State the blood parasite species.
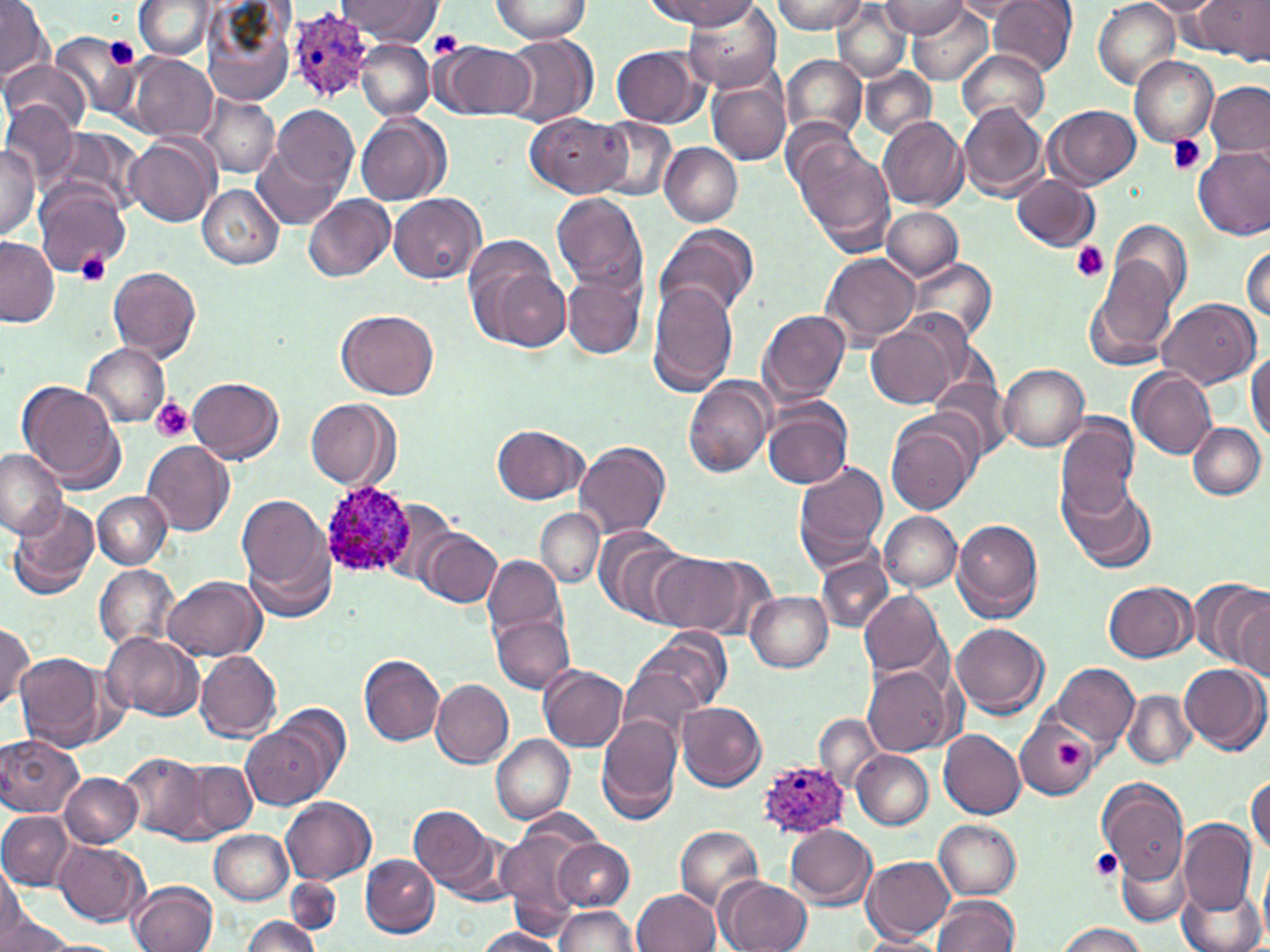
Plasmodium ovale.

Approximate bounding boxes as named x1/y1/x2/y2 corners in pixels. Plasmodium ovale-infected red blood cell locations: (x1=289, y1=6, x2=379, y2=100), (x1=317, y1=482, x2=418, y2=579), (x1=754, y1=757, x2=850, y2=841). Uninfected red blood cell locations: (x1=338, y1=0, x2=441, y2=43), (x1=490, y1=0, x2=591, y2=42), (x1=647, y1=0, x2=764, y2=29), (x1=772, y1=0, x2=868, y2=34), (x1=953, y1=0, x2=1038, y2=20), (x1=989, y1=0, x2=1077, y2=76), (x1=1138, y1=0, x2=1227, y2=17), (x1=1195, y1=0, x2=1267, y2=61), (x1=0, y1=1, x2=52, y2=81), (x1=133, y1=1, x2=215, y2=61), (x1=1093, y1=2, x2=1180, y2=86), (x1=199, y1=3, x2=295, y2=108), (x1=685, y1=3, x2=782, y2=91), (x1=831, y1=3, x2=910, y2=82), (x1=878, y1=3, x2=969, y2=36), (x1=904, y1=4, x2=995, y2=83), (x1=50, y1=30, x2=143, y2=121), (x1=502, y1=34, x2=597, y2=128), (x1=356, y1=39, x2=435, y2=121), (x1=434, y1=40, x2=533, y2=121), (x1=611, y1=46, x2=707, y2=126), (x1=957, y1=49, x2=1049, y2=130), (x1=127, y1=53, x2=219, y2=141), (x1=782, y1=54, x2=869, y2=143), (x1=1128, y1=55, x2=1217, y2=146), (x1=1, y1=58, x2=86, y2=135), (x1=861, y1=66, x2=937, y2=140), (x1=708, y1=77, x2=791, y2=165), (x1=1206, y1=81, x2=1270, y2=157), (x1=195, y1=94, x2=278, y2=178), (x1=0, y1=103, x2=80, y2=190), (x1=957, y1=103, x2=1049, y2=201), (x1=1045, y1=104, x2=1140, y2=188), (x1=270, y1=105, x2=357, y2=194), (x1=526, y1=111, x2=632, y2=197), (x1=356, y1=113, x2=450, y2=206), (x1=878, y1=115, x2=969, y2=210), (x1=780, y1=116, x2=870, y2=209), (x1=593, y1=119, x2=677, y2=202), (x1=46, y1=126, x2=144, y2=220), (x1=124, y1=132, x2=219, y2=228), (x1=794, y1=138, x2=894, y2=254), (x1=659, y1=142, x2=743, y2=227), (x1=0, y1=143, x2=41, y2=240), (x1=1194, y1=144, x2=1270, y2=240), (x1=252, y1=148, x2=342, y2=229), (x1=1012, y1=174, x2=1102, y2=253), (x1=34, y1=181, x2=134, y2=277), (x1=197, y1=184, x2=284, y2=271), (x1=552, y1=191, x2=648, y2=294), (x1=388, y1=192, x2=487, y2=285), (x1=305, y1=195, x2=394, y2=281), (x1=882, y1=208, x2=964, y2=281), (x1=1110, y1=218, x2=1193, y2=313), (x1=655, y1=223, x2=758, y2=321), (x1=0, y1=237, x2=57, y2=325), (x1=463, y1=237, x2=569, y2=351), (x1=1242, y1=240, x2=1270, y2=326), (x1=820, y1=252, x2=921, y2=347), (x1=907, y1=257, x2=998, y2=345), (x1=1089, y1=259, x2=1179, y2=366), (x1=108, y1=266, x2=201, y2=361), (x1=561, y1=269, x2=648, y2=360), (x1=646, y1=280, x2=740, y2=393), (x1=1156, y1=299, x2=1260, y2=390), (x1=758, y1=308, x2=852, y2=408), (x1=337, y1=309, x2=439, y2=401), (x1=865, y1=315, x2=967, y2=410), (x1=83, y1=344, x2=172, y2=428), (x1=1246, y1=349, x2=1270, y2=442), (x1=998, y1=365, x2=1089, y2=452), (x1=1128, y1=367, x2=1217, y2=460), (x1=186, y1=375, x2=284, y2=464), (x1=928, y1=375, x2=1015, y2=464), (x1=683, y1=377, x2=775, y2=478), (x1=17, y1=380, x2=125, y2=492), (x1=304, y1=396, x2=400, y2=490), (x1=761, y1=401, x2=851, y2=490), (x1=1055, y1=413, x2=1141, y2=516), (x1=886, y1=414, x2=978, y2=515), (x1=1189, y1=421, x2=1266, y2=499), (x1=492, y1=424, x2=588, y2=504), (x1=142, y1=440, x2=235, y2=535), (x1=574, y1=441, x2=671, y2=539), (x1=0, y1=450, x2=66, y2=537), (x1=794, y1=461, x2=889, y2=568), (x1=1059, y1=475, x2=1158, y2=575), (x1=94, y1=491, x2=171, y2=568), (x1=238, y1=494, x2=332, y2=601), (x1=381, y1=498, x2=461, y2=589), (x1=6, y1=500, x2=98, y2=598), (x1=535, y1=508, x2=603, y2=588), (x1=878, y1=512, x2=963, y2=591), (x1=952, y1=520, x2=1043, y2=623), (x1=591, y1=528, x2=698, y2=625), (x1=421, y1=529, x2=502, y2=608), (x1=650, y1=554, x2=754, y2=635), (x1=483, y1=555, x2=566, y2=640), (x1=816, y1=555, x2=892, y2=633), (x1=94, y1=564, x2=179, y2=653), (x1=162, y1=575, x2=267, y2=662), (x1=1189, y1=579, x2=1270, y2=671), (x1=1104, y1=582, x2=1198, y2=662), (x1=858, y1=589, x2=947, y2=680), (x1=746, y1=592, x2=832, y2=673), (x1=1228, y1=592, x2=1269, y2=679), (x1=490, y1=613, x2=573, y2=694), (x1=0, y1=622, x2=36, y2=709), (x1=950, y1=622, x2=1048, y2=718), (x1=637, y1=628, x2=731, y2=715), (x1=102, y1=631, x2=204, y2=721), (x1=16, y1=652, x2=107, y2=749), (x1=196, y1=652, x2=281, y2=743), (x1=359, y1=655, x2=445, y2=745), (x1=1179, y1=661, x2=1269, y2=755), (x1=1051, y1=663, x2=1139, y2=750), (x1=538, y1=664, x2=628, y2=751), (x1=865, y1=665, x2=955, y2=756), (x1=619, y1=667, x2=703, y2=748), (x1=430, y1=679, x2=514, y2=768), (x1=1122, y1=690, x2=1196, y2=769), (x1=271, y1=700, x2=349, y2=794), (x1=677, y1=702, x2=766, y2=790), (x1=595, y1=714, x2=683, y2=821), (x1=814, y1=714, x2=885, y2=792), (x1=1016, y1=719, x2=1098, y2=798), (x1=242, y1=720, x2=331, y2=809), (x1=937, y1=728, x2=1026, y2=818), (x1=1, y1=734, x2=85, y2=817), (x1=491, y1=735, x2=574, y2=823), (x1=852, y1=751, x2=933, y2=829), (x1=122, y1=753, x2=211, y2=839), (x1=190, y1=755, x2=269, y2=891), (x1=182, y1=761, x2=256, y2=839), (x1=60, y1=772, x2=143, y2=848), (x1=1247, y1=776, x2=1269, y2=854), (x1=1100, y1=779, x2=1190, y2=889), (x1=281, y1=796, x2=375, y2=884), (x1=409, y1=806, x2=497, y2=892), (x1=523, y1=809, x2=602, y2=852), (x1=1, y1=812, x2=78, y2=889), (x1=935, y1=819, x2=1022, y2=899), (x1=1179, y1=819, x2=1257, y2=916), (x1=786, y1=825, x2=878, y2=908), (x1=675, y1=826, x2=764, y2=910), (x1=498, y1=829, x2=588, y2=926), (x1=208, y1=830, x2=292, y2=904), (x1=553, y1=839, x2=635, y2=910), (x1=54, y1=840, x2=149, y2=927), (x1=1115, y1=841, x2=1192, y2=928), (x1=361, y1=854, x2=439, y2=938), (x1=862, y1=855, x2=956, y2=943), (x1=0, y1=866, x2=34, y2=943), (x1=716, y1=875, x2=811, y2=952), (x1=285, y1=877, x2=341, y2=936), (x1=129, y1=880, x2=216, y2=952), (x1=1177, y1=885, x2=1265, y2=952), (x1=631, y1=889, x2=719, y2=952), (x1=933, y1=896, x2=1020, y2=952), (x1=552, y1=905, x2=639, y2=952), (x1=0, y1=910, x2=74, y2=952), (x1=241, y1=915, x2=319, y2=952), (x1=1053, y1=922, x2=1147, y2=952), (x1=474, y1=927, x2=566, y2=952), (x1=857, y1=933, x2=945, y2=952). Platelet locations: (x1=430, y1=30, x2=464, y2=58), (x1=103, y1=37, x2=140, y2=70), (x1=1166, y1=134, x2=1209, y2=177), (x1=1071, y1=242, x2=1109, y2=282), (x1=76, y1=252, x2=111, y2=286), (x1=151, y1=398, x2=192, y2=442), (x1=1055, y1=742, x2=1084, y2=766), (x1=1090, y1=848, x2=1122, y2=881). Thin blood smear. Single field of view. Optical microscopy. 1000x magnification. May-Grünwald-Giemsa stain. Image is 1270×952 pixels.